Give the position of every Plasmodium parasite visible.
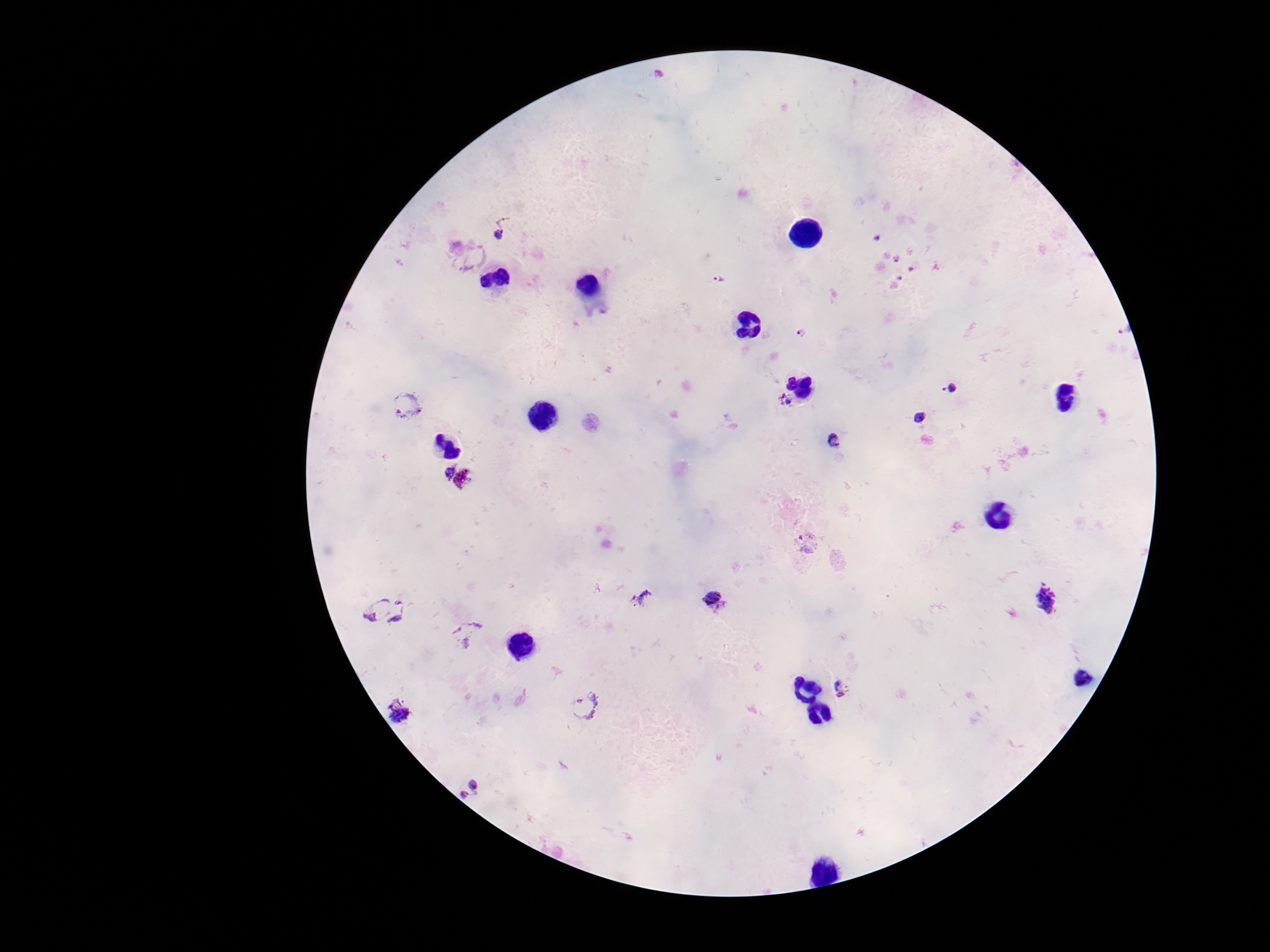
Approximate object centers, in pixels from the top-left corner.
Plasmodium parasites: (x=503, y=227), (x=877, y=238), (x=471, y=255), (x=898, y=260), (x=913, y=269), (x=899, y=278), (x=720, y=280), (x=800, y=333), (x=951, y=387), (x=784, y=400), (x=407, y=406), (x=920, y=418), (x=833, y=440), (x=445, y=472), (x=466, y=480), (x=807, y=541), (x=643, y=597), (x=1046, y=598), (x=365, y=599), (x=717, y=603), (x=406, y=616), (x=468, y=633), (x=845, y=687), (x=586, y=706), (x=399, y=712), (x=469, y=790).

Giemsa-stained preparation. Single field of view. Image is 1270×952 pixels. Patient malaria status: infected. Thick blood film. Photographed through the microscope eyepiece with a smartphone camera. 100x magnification.